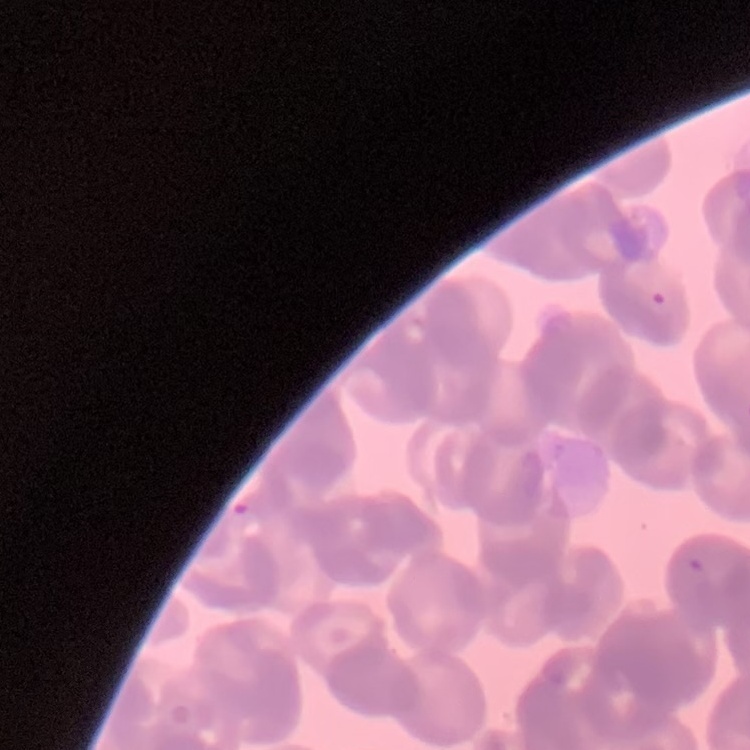
Summary:
  - Erythrocyte morphology: rouleaux formation
  - Image type: one tile cut from a larger photomicrograph
  - Preparation: thin blood film
  - Stain: Field's or Giemsa